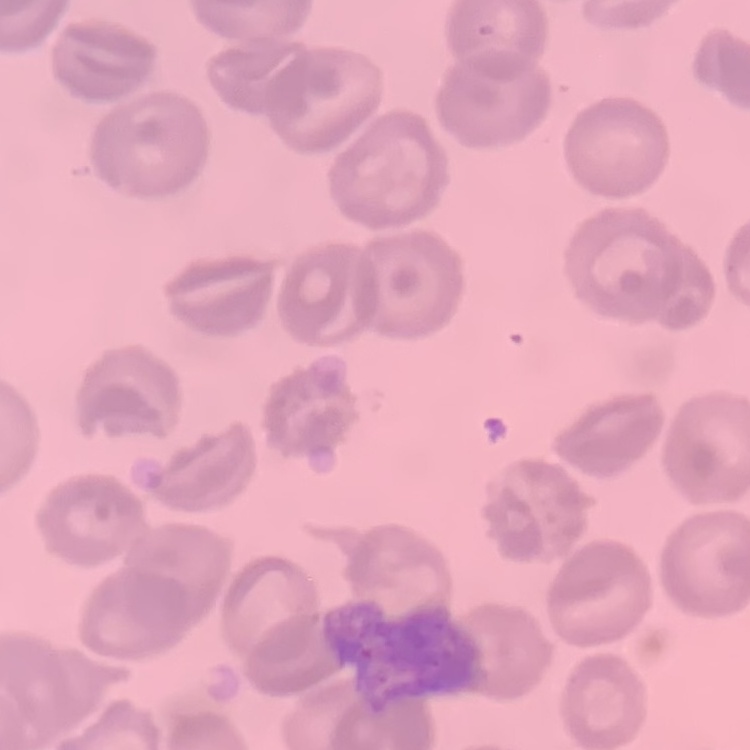

Summary:
  - Red blood cell morphology: no rouleaux formation
  - Preparation: thin peripheral smear
  - Stain: Field's or Giemsa
  - Image type: square crop of a larger photomicrograph